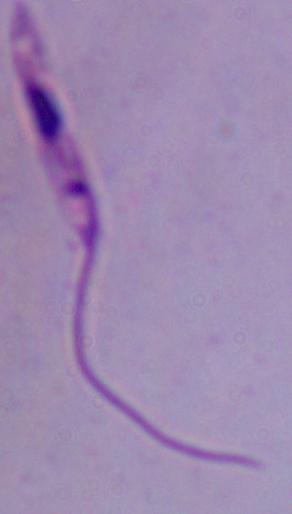

modality: photomicrograph
magnification: 1000x
identification: Leishmania